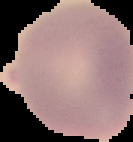
result: no Plasmodium parasites seen
preparation: thin blood film
image_size: 133×142 pixels
image_type: segmented cell region on a black background